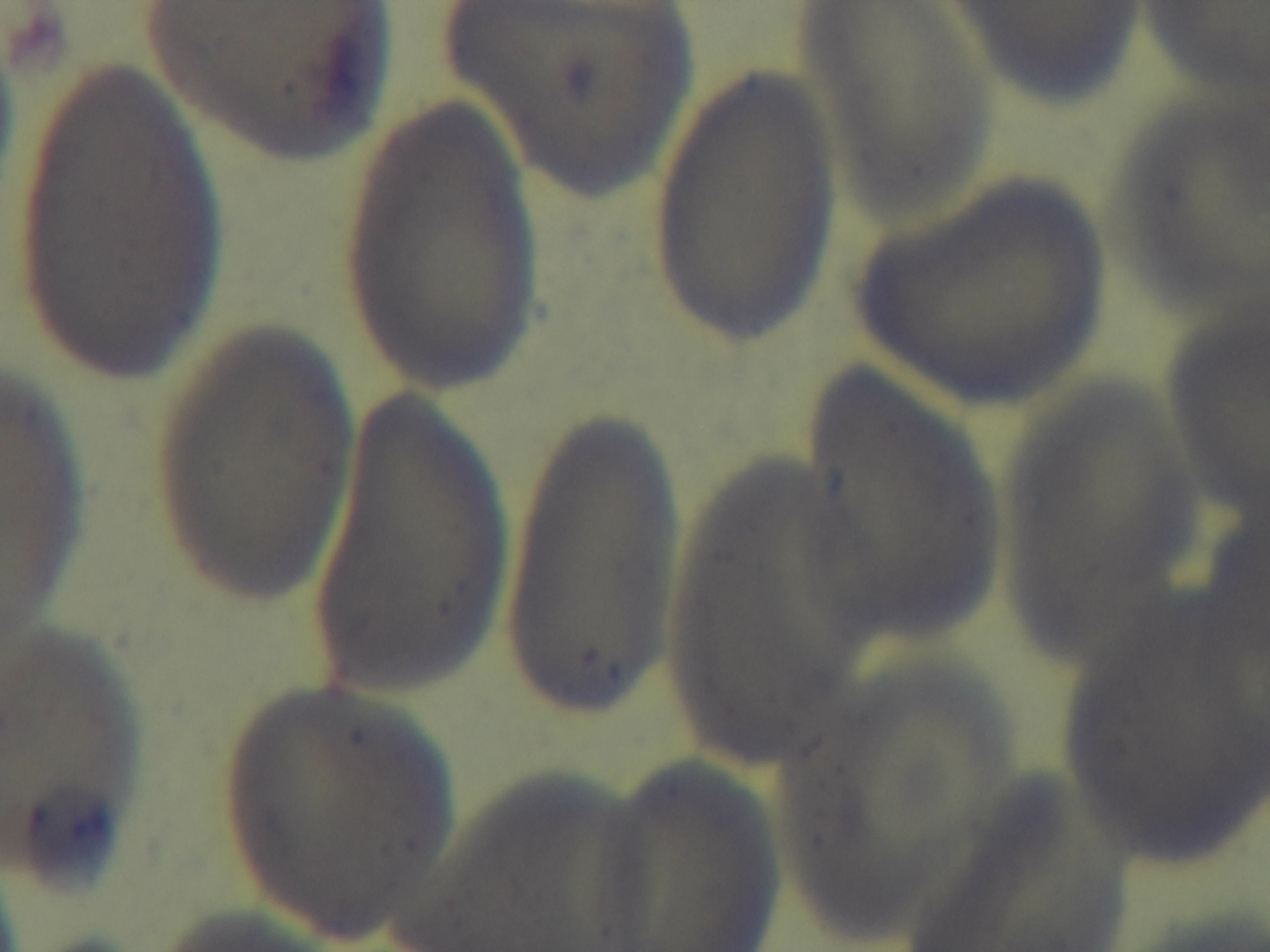

Summary:
  - Malaria status: uninfected
  - Capture: mounted 4K digital camera
  - Modality: light microscopy
  - Stain: Giemsa
  - Objective: 100x oil immersion
  - Preparation: thin blood film
  - Field of view: single